Outline each uninfected red blood cell.
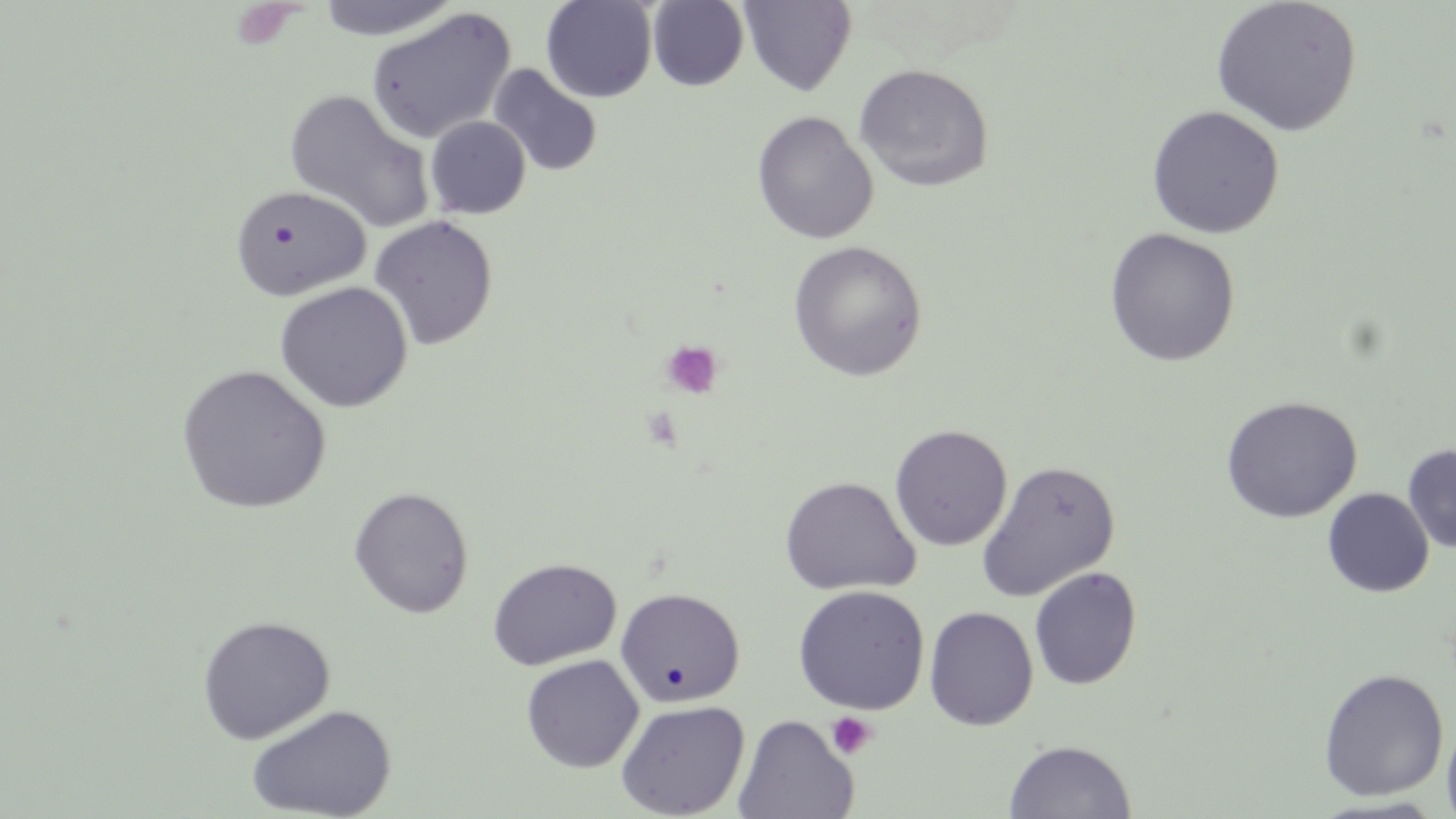
Approximate bounding boxes as [x1, y1, x2, y2] in pixels.
Uninfected red blood cells: [314, 0, 462, 41], [541, 0, 657, 103], [1211, 0, 1363, 137], [648, 1, 749, 91], [739, 1, 856, 95], [366, 7, 516, 143], [854, 63, 994, 192], [487, 64, 603, 178], [281, 85, 433, 232], [1146, 105, 1285, 239], [752, 111, 878, 244], [425, 116, 531, 220], [230, 184, 372, 300], [368, 215, 499, 351], [1104, 228, 1240, 366], [788, 241, 927, 381], [274, 281, 413, 413], [176, 364, 331, 514], [1220, 395, 1363, 523], [890, 424, 1013, 552], [1403, 444, 1456, 554], [977, 460, 1120, 602], [779, 475, 921, 597], [348, 486, 474, 619], [1323, 488, 1434, 597], [487, 557, 622, 671], [1029, 567, 1142, 691], [793, 585, 929, 714], [615, 587, 746, 708], [923, 607, 1038, 731], [197, 615, 335, 743], [520, 654, 644, 773], [1318, 668, 1449, 801], [616, 699, 750, 818], [246, 704, 397, 818], [733, 714, 859, 819], [1441, 714, 1456, 819], [1004, 739, 1137, 819].

Summary:
  - Platelet locations: [661, 340, 723, 399], [826, 712, 877, 759]
  - Slide-level diagnosis: negative for blood parasites
  - Preparation: thin blood smear
  - Magnification: 1000x
  - Field of view: single
  - Image size: 1456×819 pixels
  - Modality: light microscopy
  - Stain: May-Grünwald-Giemsa